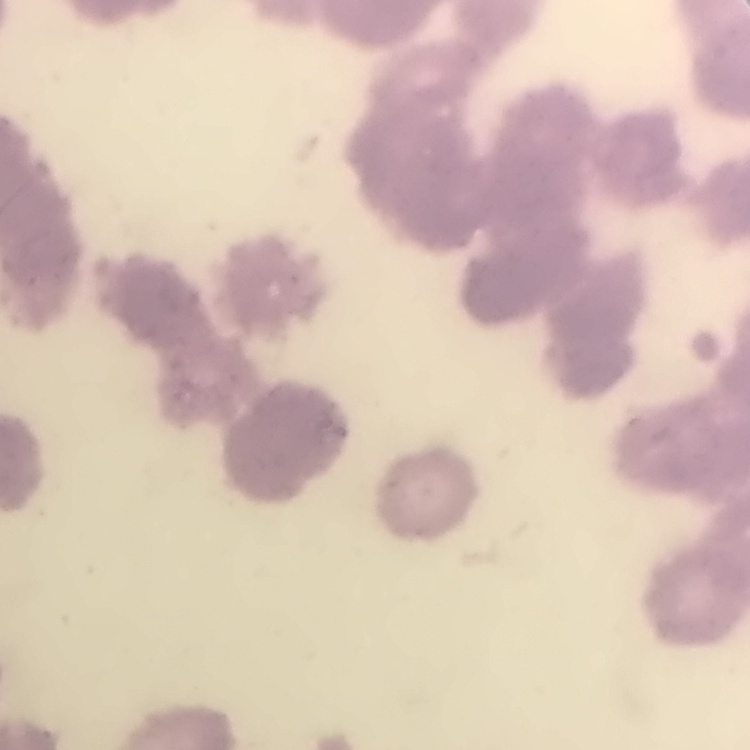
erythrocyte_morphology: rouleaux formation
stain: Field's or Giemsa
image_type: one tile cut from a larger photomicrograph
preparation: thin blood smear